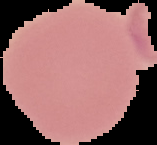
Summary:
  - Image type: segmented cell region on a black background
  - Preparation: thin blood film
  - Malaria status: uninfected
  - Image size: 157×145 pixels